Describe the morphology of the erythrocytes.
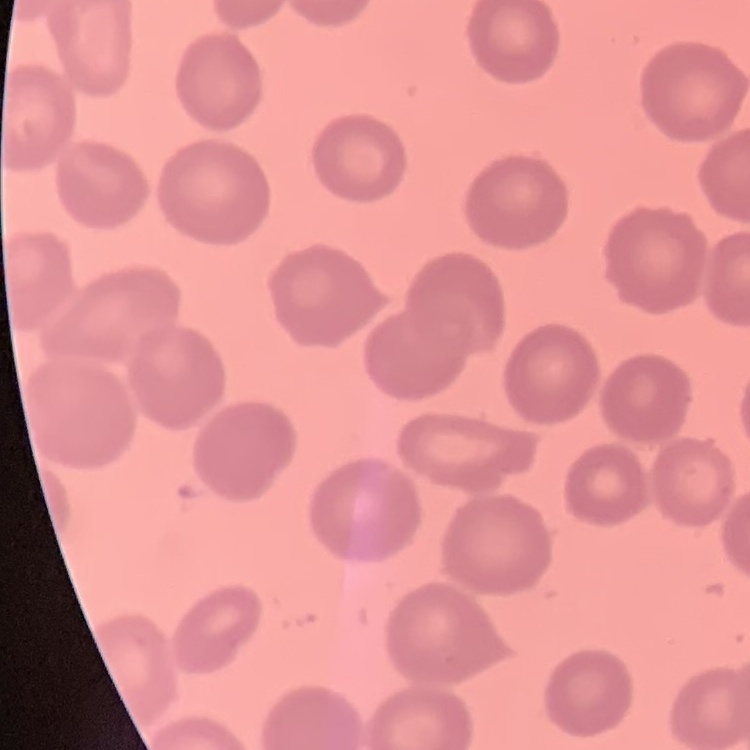
They show no rouleaux formation.

Summary:
  - Preparation: thin blood smear
  - Stain: Field's or Giemsa
  - Image type: square crop of a larger photomicrograph